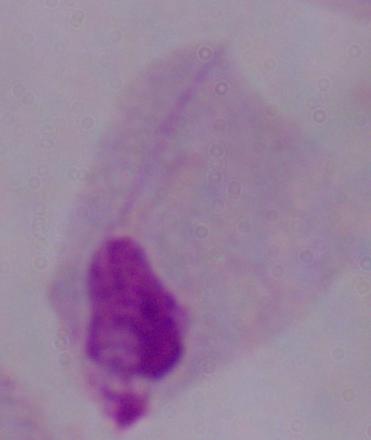
Summary:
  - Magnification: 1000x
  - Modality: micrograph
  - Identification: trichomonad